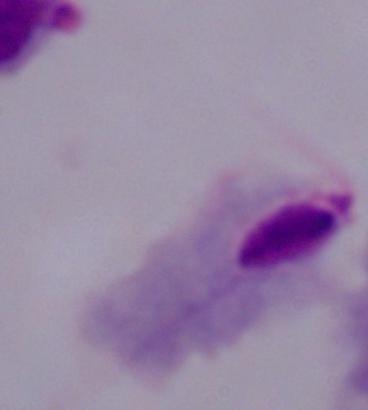
1000x magnification. A trichomonad is shown. Photomicrograph.